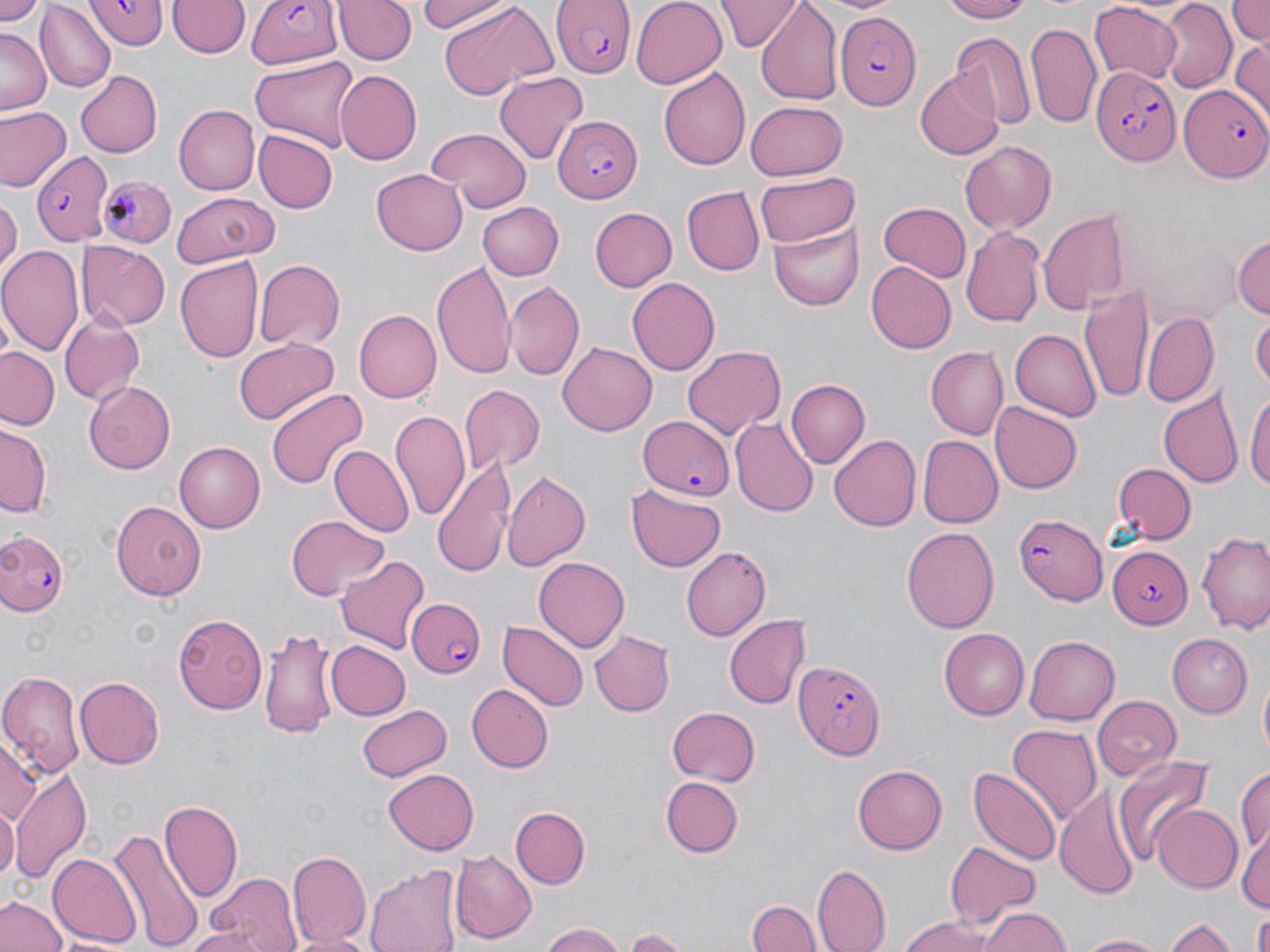
Approximate bounding boxes as (x1,y1)-(x2,y2) corner pairs in pixels. Uninfected red blood cell locations: (0,0)-(46,25), (332,0)-(415,65), (630,0)-(725,89), (717,0)-(798,52), (818,0)-(903,15), (940,0)-(1030,24), (1159,0)-(1237,91), (1227,0)-(1270,49), (36,1)-(115,92), (168,1)-(248,58), (418,1)-(516,36), (755,1)-(843,106), (1090,2)-(1183,84), (440,4)-(553,99), (1025,19)-(1101,127), (1,29)-(49,114), (951,31)-(1034,128), (1230,37)-(1270,124), (251,55)-(360,148), (659,66)-(749,171), (74,70)-(162,157), (334,70)-(422,165), (492,70)-(588,164), (916,70)-(1002,161), (744,101)-(848,180), (174,105)-(259,195), (1,107)-(70,192), (424,127)-(534,212), (252,129)-(338,213), (959,141)-(1057,234), (373,167)-(468,254), (754,175)-(860,246), (681,185)-(765,277), (0,192)-(22,279), (171,195)-(281,266), (477,202)-(562,281), (878,202)-(972,284), (589,208)-(678,293), (1038,209)-(1131,315), (769,220)-(864,312), (962,225)-(1044,326), (1232,234)-(1269,321), (76,239)-(169,331), (0,245)-(84,356), (174,258)-(263,365), (254,259)-(345,351), (431,262)-(517,378), (866,263)-(955,354), (627,276)-(720,378), (506,280)-(586,380), (1081,283)-(1155,409), (356,308)-(443,403), (1142,310)-(1219,408), (1251,311)-(1269,395), (59,313)-(145,407), (1009,329)-(1100,420), (235,337)-(332,421), (558,340)-(657,437), (682,344)-(784,440), (1,347)-(61,430), (926,347)-(1008,438), (787,379)-(869,466), (85,382)-(176,473), (457,384)-(543,474), (1247,387)-(1270,500), (264,389)-(367,492), (1157,389)-(1243,492), (991,402)-(1083,493), (391,409)-(470,520), (731,418)-(818,518), (0,427)-(48,520), (831,434)-(922,532), (917,436)-(1003,529), (174,442)-(266,533), (329,444)-(413,537), (432,455)-(517,575), (1112,464)-(1194,544), (502,469)-(591,570), (625,486)-(728,573), (110,500)-(206,598), (285,515)-(389,602), (901,526)-(1000,634), (1196,530)-(1270,631), (680,546)-(771,642), (334,555)-(431,653), (534,555)-(629,651), (171,612)-(267,713), (725,614)-(811,711), (500,621)-(587,713), (941,626)-(1032,719), (259,627)-(341,738), (587,631)-(676,718), (1170,634)-(1253,718), (1024,635)-(1119,725), (326,641)-(411,720), (0,673)-(84,774), (1257,673)-(1270,764), (75,676)-(163,769), (468,684)-(552,774), (1092,696)-(1181,781), (356,702)-(450,781), (667,707)-(761,785), (1007,724)-(1102,829), (0,735)-(37,828), (1112,752)-(1220,866), (852,764)-(945,854), (1234,764)-(1270,859), (969,765)-(1062,866), (12,767)-(90,881), (383,769)-(480,855), (661,777)-(743,858), (1055,784)-(1142,897), (159,801)-(242,906), (0,802)-(18,881), (1152,803)-(1243,893), (511,805)-(589,888), (1236,823)-(1270,913), (108,826)-(205,952), (946,840)-(1039,924), (454,847)-(538,943), (286,848)-(370,949), (46,850)-(141,949), (367,864)-(461,952), (813,864)-(890,952), (203,873)-(303,952), (1,894)-(68,952), (748,897)-(819,952), (982,907)-(1072,952), (1166,913)-(1237,952), (1248,913)-(1270,952), (899,916)-(994,952), (626,924)-(690,950), (178,925)-(273,952), (541,925)-(626,952), (289,930)-(375,952), (1076,933)-(1169,952). Plasmodium falciparum-infected red blood cell locations: (85,0)-(166,48), (247,0)-(343,71), (551,0)-(636,79), (836,13)-(923,111), (1090,67)-(1180,166), (1178,85)-(1270,183), (550,114)-(641,202), (29,151)-(114,245), (99,175)-(175,250), (638,415)-(734,498), (1014,509)-(1107,604), (0,528)-(70,619), (1105,544)-(1194,628), (411,597)-(488,680), (792,656)-(885,760). Slide-level diagnosis: Plasmodium falciparum. Single field of view. Light microscopy. Captured at 1000x magnification. Image is 1270×952 pixels. May-Grünwald-Giemsa-stained preparation. Thin blood film.